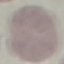

malaria status = uninfected
stain = Giemsa
image type = automatically extracted cell patch, resized to 64 × 64 pixels
capture = smartphone through the microscope eyepiece
preparation = thin blood film